Assess the morphology of the red blood cells.
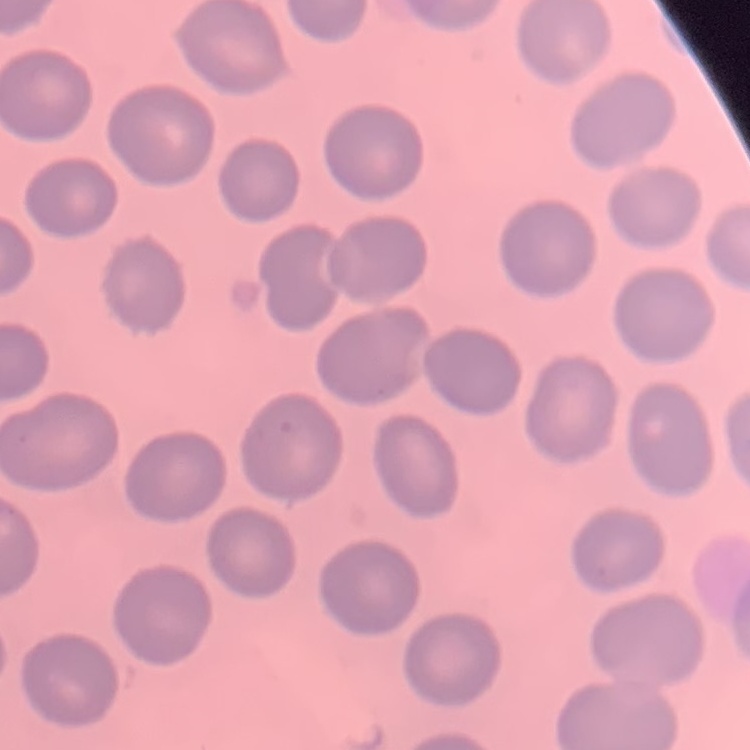
They show no rouleaux formation.

Stained with either Field's or Giemsa. One tile cut from a larger photomicrograph. Thin blood film.